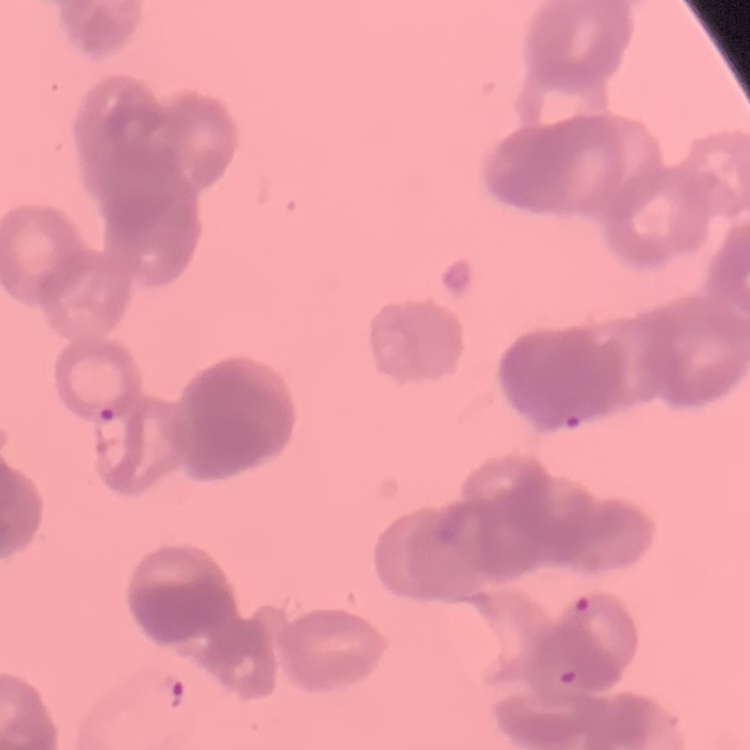

The erythrocytes exhibit rouleaux formation. One tile cut from a larger photomicrograph. Field's or Giemsa stain. Thin blood smear.